Locate every Plasmodium parasite.
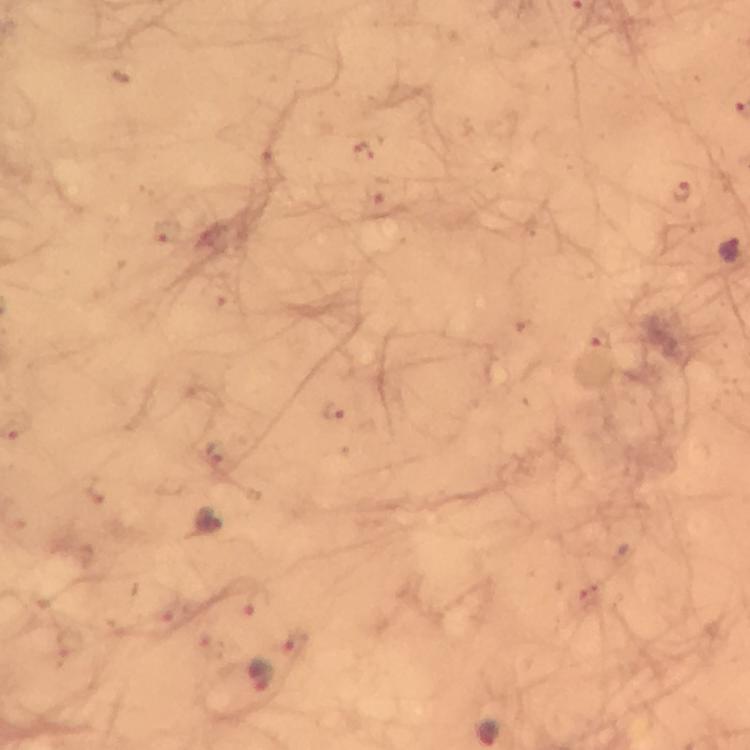
Approximate centers as (x, y) in pixels.
Plasmodium parasites: (362, 152), (681, 190), (379, 193), (167, 230), (728, 249), (599, 337), (335, 413), (217, 453), (209, 521), (257, 604), (294, 642), (260, 676).

image size = 750×750 pixels
immersion oil = used
context = from a malaria diagnostic workup
capture = smartphone mounted on the microscope
magnification = 100x
stain = Giemsa
cropped from = a single field of view
preparation = thick blood film